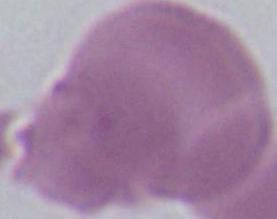

Summary:
  - Identification: red blood cell
  - Magnification: 1000x
  - Modality: photomicrograph